Report the malaria status of this cell.
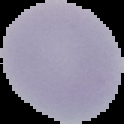

It is uninfected.

Cell region segmented out of the field of view; the surrounding area is masked to black. Image is 124×124 pixels. From a thin blood smear.